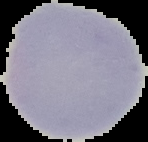
image size = 148×142 pixels
image type = cell region segmented out of the field of view; surrounding area masked to black
preparation = thin blood smear
result = no Plasmodium parasites seen